State the blood parasite species.
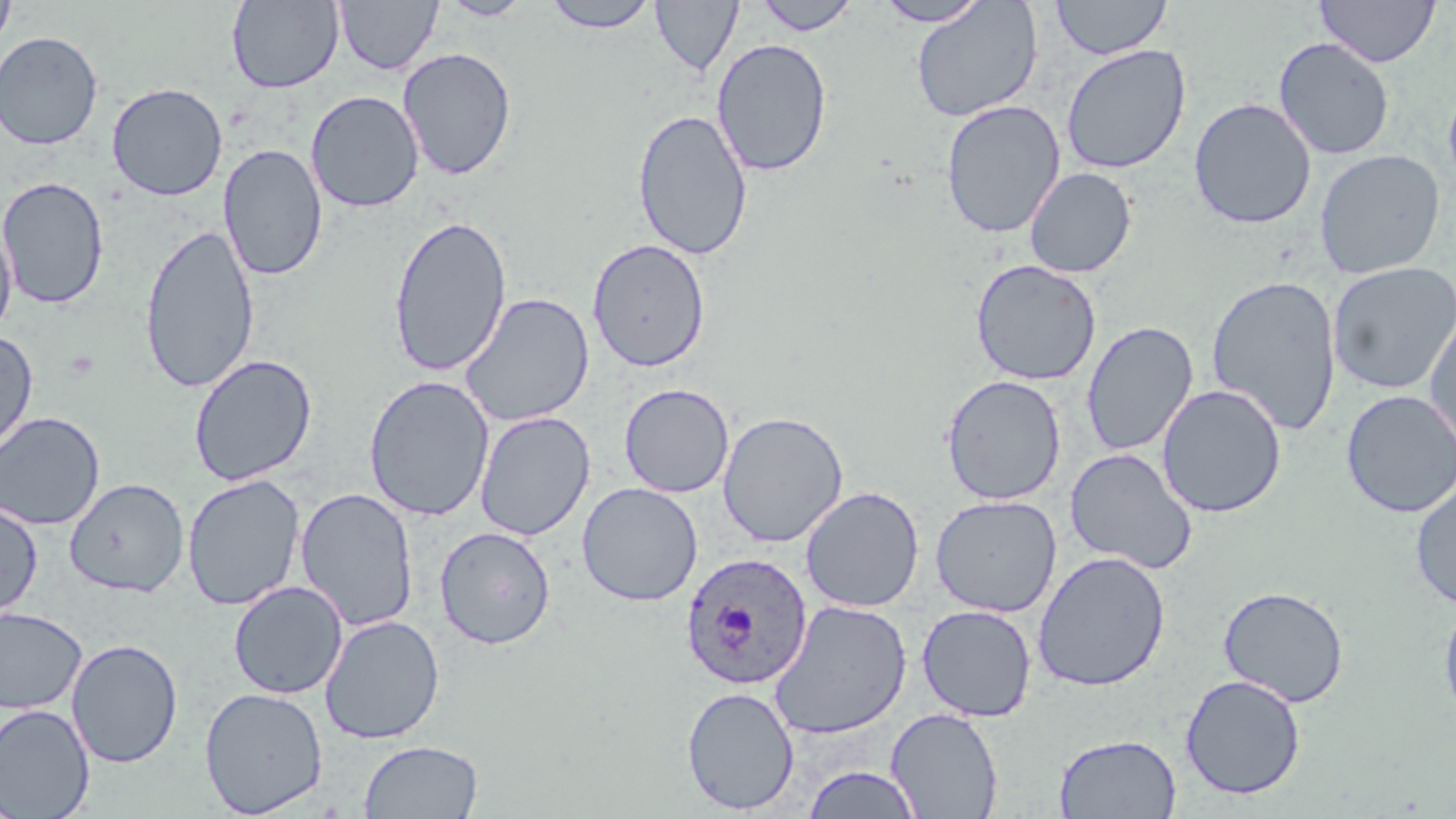
Plasmodium ovale.

magnification = 1000x
image size = 1456×819 pixels
field of view = one of a larger specimen
stain = May-Grünwald-Giemsa
modality = optical microscopy
preparation = thin blood smear
uninfected red blood cell locations = approximate bounding boxes as named x1/y1/x2/y2 corners in pixels: (x1=1, y1=0, x2=16, y2=54), (x1=227, y1=0, x2=344, y2=93), (x1=335, y1=0, x2=442, y2=75), (x1=541, y1=0, x2=659, y2=33), (x1=754, y1=0, x2=860, y2=35), (x1=874, y1=0, x2=990, y2=26), (x1=1051, y1=0, x2=1171, y2=60), (x1=1315, y1=0, x2=1440, y2=67), (x1=439, y1=1, x2=533, y2=21), (x1=650, y1=1, x2=743, y2=76), (x1=912, y1=1, x2=1042, y2=123), (x1=0, y1=30, x2=104, y2=150), (x1=711, y1=37, x2=832, y2=177), (x1=1274, y1=37, x2=1395, y2=160), (x1=1060, y1=44, x2=1191, y2=174), (x1=397, y1=47, x2=517, y2=180), (x1=1443, y1=79, x2=1456, y2=197), (x1=106, y1=82, x2=228, y2=201), (x1=305, y1=90, x2=424, y2=213), (x1=1189, y1=98, x2=1316, y2=230), (x1=941, y1=99, x2=1066, y2=239), (x1=632, y1=108, x2=753, y2=262), (x1=219, y1=143, x2=327, y2=282), (x1=1314, y1=150, x2=1445, y2=279), (x1=1024, y1=167, x2=1136, y2=278), (x1=0, y1=176, x2=109, y2=309), (x1=388, y1=214, x2=512, y2=377), (x1=0, y1=216, x2=17, y2=341), (x1=140, y1=222, x2=259, y2=394), (x1=587, y1=239, x2=711, y2=372), (x1=970, y1=259, x2=1102, y2=385), (x1=1327, y1=261, x2=1456, y2=395), (x1=1206, y1=275, x2=1341, y2=436), (x1=459, y1=292, x2=595, y2=428), (x1=1424, y1=309, x2=1456, y2=458), (x1=1081, y1=321, x2=1198, y2=456), (x1=0, y1=330, x2=38, y2=458), (x1=189, y1=353, x2=318, y2=486), (x1=940, y1=374, x2=1066, y2=505), (x1=364, y1=375, x2=495, y2=522), (x1=619, y1=383, x2=735, y2=498), (x1=1156, y1=384, x2=1287, y2=518), (x1=1340, y1=389, x2=1456, y2=519), (x1=0, y1=411, x2=105, y2=531), (x1=474, y1=411, x2=595, y2=541), (x1=717, y1=411, x2=849, y2=547), (x1=1064, y1=448, x2=1199, y2=575), (x1=182, y1=473, x2=305, y2=611), (x1=1410, y1=476, x2=1456, y2=611), (x1=65, y1=478, x2=188, y2=597), (x1=577, y1=482, x2=703, y2=606), (x1=800, y1=486, x2=924, y2=613), (x1=295, y1=487, x2=419, y2=631), (x1=929, y1=495, x2=1062, y2=617), (x1=0, y1=499, x2=43, y2=623), (x1=434, y1=525, x2=556, y2=649), (x1=1032, y1=551, x2=1170, y2=692), (x1=228, y1=580, x2=347, y2=699), (x1=1218, y1=586, x2=1349, y2=708), (x1=1438, y1=594, x2=1456, y2=725), (x1=770, y1=600, x2=912, y2=740), (x1=916, y1=604, x2=1038, y2=722), (x1=0, y1=606, x2=88, y2=714), (x1=320, y1=614, x2=445, y2=744), (x1=66, y1=638, x2=183, y2=768), (x1=1180, y1=674, x2=1306, y2=800), (x1=199, y1=686, x2=328, y2=817), (x1=682, y1=686, x2=800, y2=814), (x1=0, y1=703, x2=95, y2=818), (x1=886, y1=707, x2=1003, y2=819), (x1=1054, y1=733, x2=1181, y2=818), (x1=359, y1=740, x2=483, y2=818), (x1=802, y1=766, x2=923, y2=819)
Plasmodium ovale-infected red blood cell locations = approximate bounding boxes as named x1/y1/x2/y2 corners in pixels: (x1=680, y1=552, x2=813, y2=690)